Name the cell type shown.
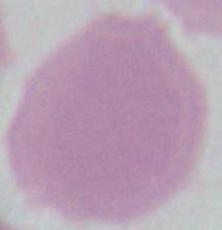

An erythrocyte.

1000x magnification. Photomicrograph.